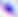

magnification = 400x
identification = Toxoplasma gondii
modality = photomicrograph